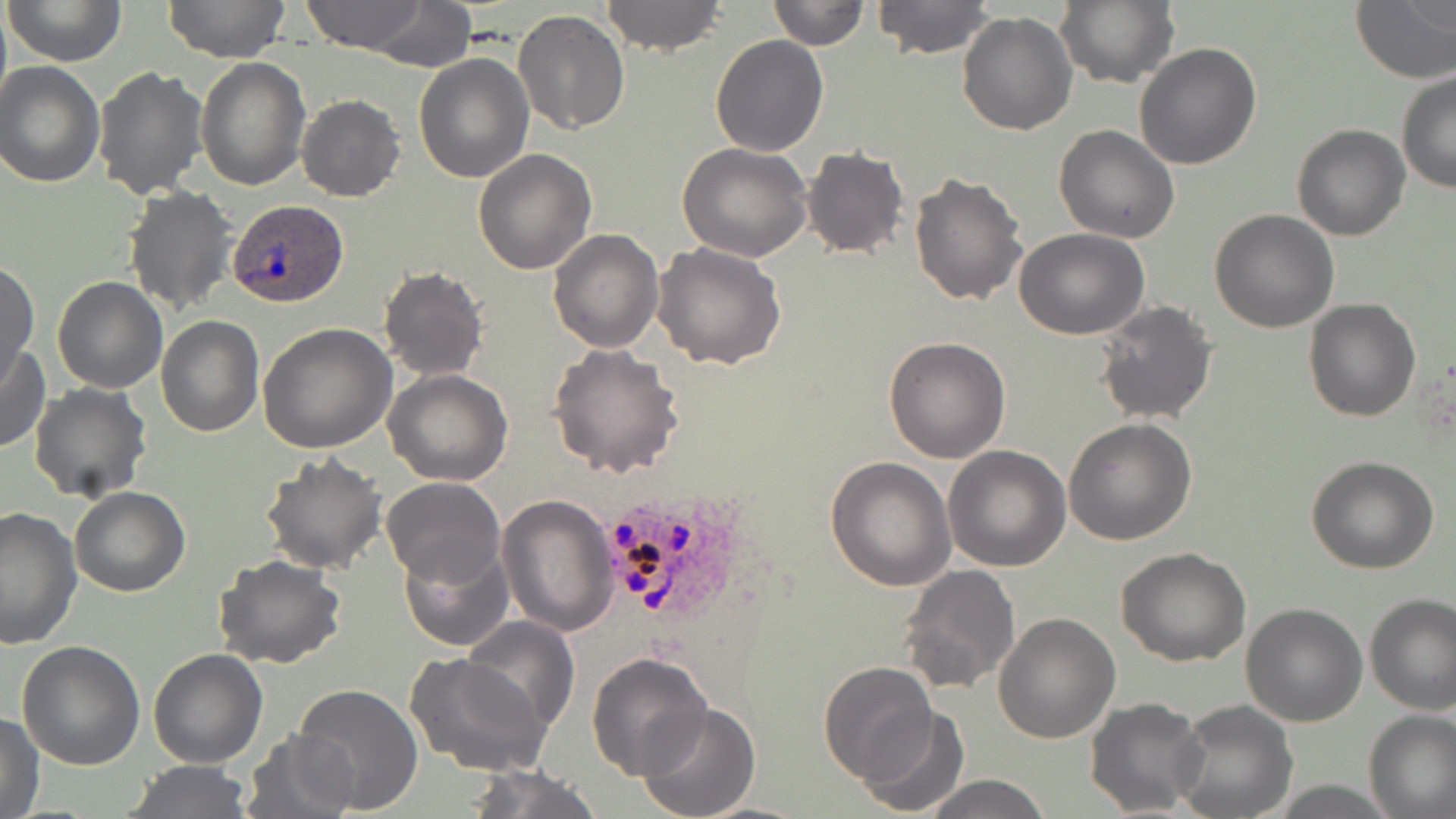
Summary:
  - Coordinate format: approximate bounding boxes as [x1, y1, x2, y2] in pixels
  - Plasmodium ovale-infected red blood cell locations: [227, 201, 345, 307], [612, 496, 710, 621]
  - Uninfected red blood cell locations: [5, 0, 126, 68], [163, 0, 292, 65], [300, 0, 432, 52], [599, 0, 728, 56], [768, 0, 867, 50], [871, 0, 995, 57], [1054, 0, 1179, 88], [1350, 0, 1456, 84], [348, 3, 477, 69], [513, 8, 630, 136], [956, 10, 1077, 136], [711, 34, 828, 155], [1133, 42, 1262, 170], [413, 51, 532, 183], [195, 56, 309, 191], [0, 61, 105, 186], [93, 66, 209, 201], [1397, 71, 1456, 193], [297, 94, 405, 202], [1054, 124, 1181, 243], [1291, 124, 1411, 241], [678, 142, 813, 261], [799, 145, 912, 261], [474, 149, 597, 275], [909, 171, 1029, 306], [123, 185, 239, 318], [1209, 209, 1340, 333], [548, 227, 664, 353], [1013, 229, 1150, 340], [651, 241, 786, 371], [0, 261, 37, 383], [377, 266, 488, 381], [51, 275, 168, 395], [1303, 298, 1422, 423], [1093, 300, 1217, 424], [156, 317, 266, 438], [257, 322, 398, 454], [883, 336, 1012, 463], [0, 343, 48, 452], [547, 344, 685, 478], [383, 368, 512, 485], [29, 384, 150, 503], [1064, 418, 1196, 544], [943, 446, 1072, 571], [258, 452, 387, 574], [1306, 454, 1439, 574], [825, 456, 955, 592], [381, 476, 506, 590], [69, 486, 192, 597], [496, 494, 618, 635], [0, 505, 81, 649], [399, 542, 513, 651], [1116, 545, 1251, 667], [212, 554, 345, 671], [896, 564, 1021, 697], [1364, 593, 1456, 713], [1240, 602, 1368, 727], [993, 611, 1120, 743], [460, 615, 581, 736], [17, 641, 146, 770], [147, 648, 268, 768], [586, 652, 713, 777], [404, 653, 554, 780], [819, 661, 939, 784], [291, 684, 423, 811], [1085, 697, 1208, 817], [1169, 699, 1297, 819], [636, 702, 763, 819], [855, 706, 971, 818], [1364, 708, 1456, 817], [1, 710, 44, 818], [241, 729, 361, 819], [124, 759, 255, 817], [459, 762, 603, 819], [921, 775, 1055, 818]
  - Slide-level diagnosis: Plasmodium ovale
  - Stain: May-Grünwald-Giemsa
  - Magnification: 1000x
  - Field of view: one of a larger specimen
  - Modality: optical microscopy
  - Preparation: thin blood film
  - Image size: 1456×819 pixels